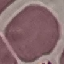

malaria status = uninfected
capture = smartphone through the microscope eyepiece
image type = cell patch, automatically extracted from a larger field of view and resized to 64 × 64 pixels
stain = Giemsa
preparation = thin blood film